Name the parasite shown.
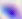
Toxoplasma gondii.

{
  "magnification": "400x",
  "modality": "micrograph"
}